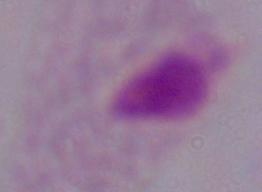

Summary:
  - Modality: photomicrograph
  - Magnification: 1000x
  - Identification: trichomonad